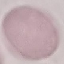
Summary:
  - Malaria status: uninfected
  - Capture: smartphone camera at the microscope eyepiece
  - Image type: cell patch, automatically extracted from a larger field of view and resized to 64 × 64 pixels
  - Stain: Giemsa
  - Preparation: thin smear